Identify the parasite.
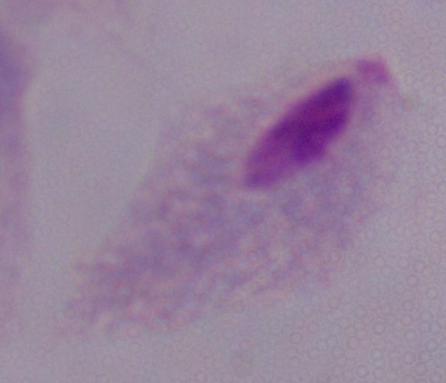
This is a trichomonad.

magnification: 1000x
modality: micrograph